Outline platelets.
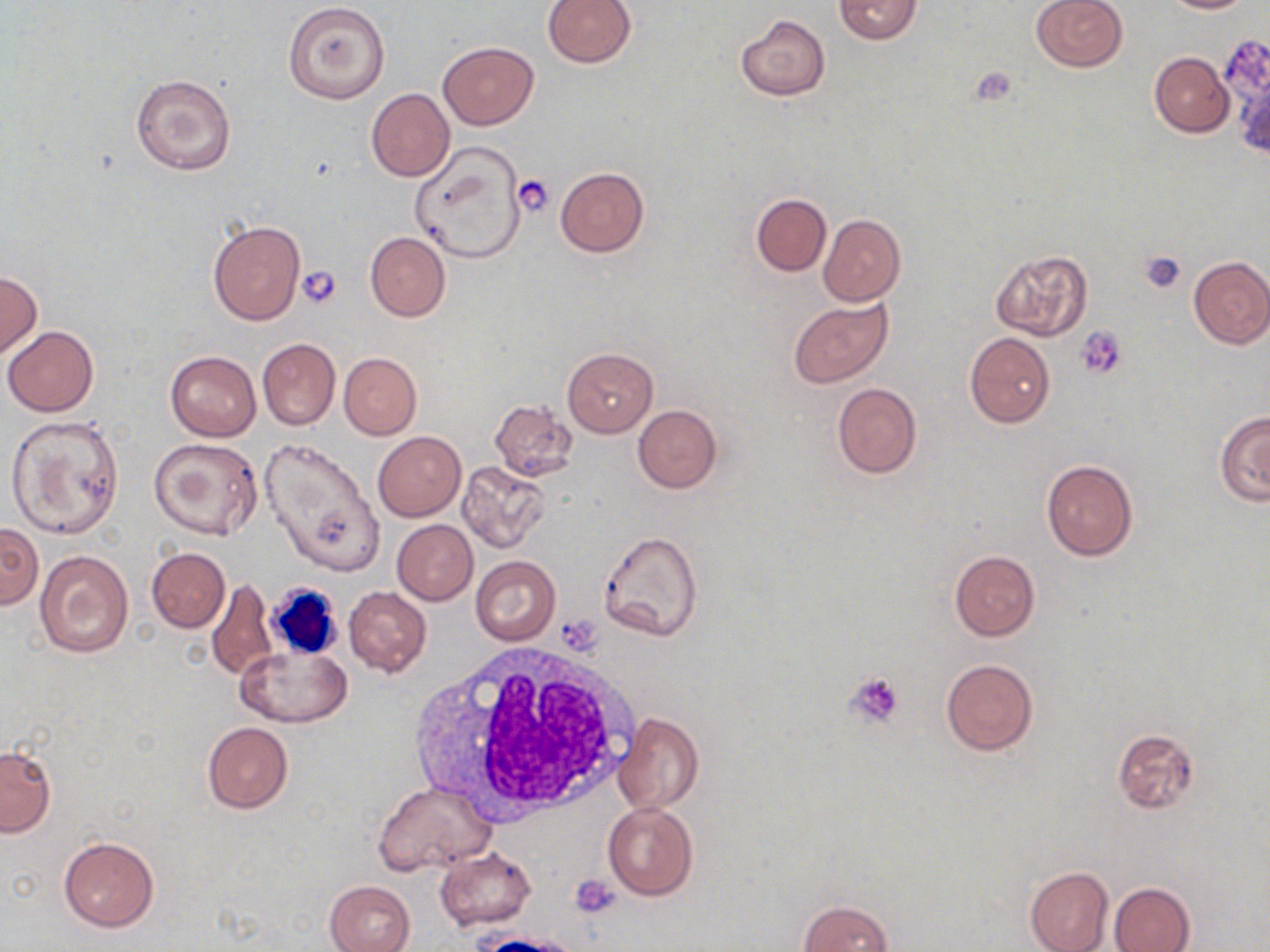
Approximate bounding boxes as (x1, y1, x2, y2) in pixels.
Platelets: (515, 174, 557, 217), (1139, 251, 1187, 293), (295, 264, 342, 309), (1075, 326, 1127, 381), (844, 671, 905, 731), (571, 876, 622, 919).

Uninfected red blood cell locations: (542, 0, 637, 68), (835, 0, 922, 44), (1031, 0, 1126, 72), (1163, 0, 1255, 14), (284, 2, 389, 104), (734, 15, 830, 100), (438, 41, 538, 130), (1149, 52, 1235, 137), (131, 73, 237, 174), (366, 88, 455, 182), (409, 142, 527, 265), (555, 167, 649, 256), (751, 193, 831, 276), (818, 214, 905, 306), (208, 221, 304, 324), (365, 232, 450, 322), (989, 249, 1093, 343), (1187, 255, 1270, 349), (0, 271, 42, 359), (788, 298, 893, 389), (3, 326, 99, 416), (964, 332, 1055, 428), (257, 338, 339, 430), (563, 347, 658, 437), (165, 350, 261, 441), (338, 352, 421, 439), (832, 383, 921, 479), (489, 399, 577, 481), (633, 404, 722, 493), (1215, 409, 1270, 505), (6, 416, 123, 538), (373, 430, 466, 520), (150, 436, 263, 541), (257, 438, 384, 577), (1041, 459, 1138, 562), (458, 462, 550, 553), (392, 519, 477, 605), (0, 522, 41, 610), (599, 529, 703, 641), (146, 547, 229, 633), (949, 549, 1040, 641), (34, 550, 135, 658), (470, 555, 561, 644), (207, 578, 276, 681), (343, 586, 432, 677), (237, 642, 351, 726), (940, 657, 1039, 757), (613, 713, 703, 816), (202, 722, 293, 813), (1112, 728, 1200, 814), (0, 745, 56, 837), (373, 780, 494, 877), (603, 801, 699, 900), (59, 837, 158, 930), (436, 847, 535, 930), (1024, 865, 1114, 952), (324, 880, 415, 952), (1109, 883, 1194, 951), (798, 900, 893, 952). White blood cell locations: (263, 582, 342, 662), (409, 642, 639, 821). Slide-level diagnosis: negative for blood parasites. Optical microscopy. Image is 1270×952 pixels. 1000x magnification. May-Grünwald-Giemsa stain. One field of a larger specimen. Thin blood film.